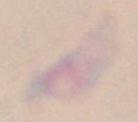
Toxoplasma gondii is seen. Photomicrograph. 1000x magnification.